State which cell type is depicted.
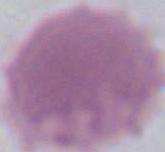

This is an erythrocyte.

Summary:
  - Magnification: 1000x
  - Modality: micrograph